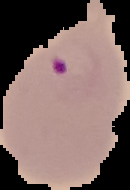
Summary:
  - Preparation: thin blood smear
  - Image size: 130×190 pixels
  - Image type: segmented cell region on a black background
  - Malaria status: parasitized